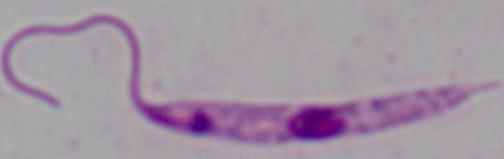

Summary:
  - Magnification: 1000x
  - Modality: micrograph
  - Identification: Leishmania